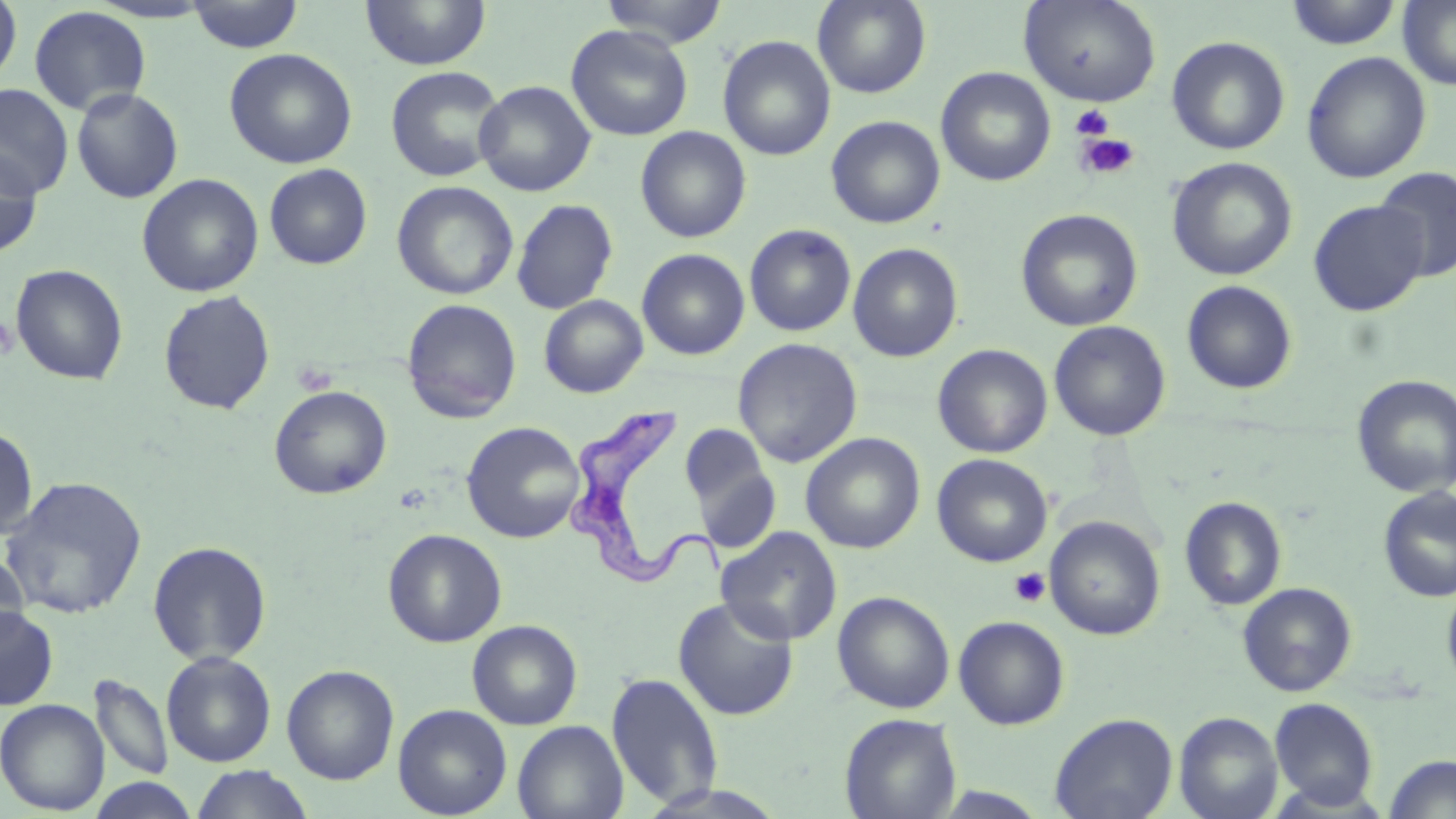
slide-level diagnosis = Trypanosoma brucei
uninfected red blood cell locations = approximate bounding boxes as [x1, y1, x2, y2] in pixels: [359, 0, 491, 71], [600, 0, 729, 48], [812, 0, 931, 98], [1284, 0, 1403, 50], [0, 1, 22, 88], [187, 1, 304, 53], [1018, 1, 1161, 107], [1398, 1, 1456, 90], [28, 5, 151, 115], [566, 24, 693, 141], [717, 35, 836, 161], [1166, 36, 1290, 155], [224, 47, 358, 169], [1301, 51, 1432, 183], [385, 65, 506, 182], [936, 66, 1056, 187], [474, 80, 596, 196], [0, 84, 74, 198], [71, 87, 184, 203], [826, 115, 945, 229], [635, 126, 751, 243], [0, 149, 42, 257], [1166, 157, 1298, 281], [263, 164, 372, 269], [1375, 166, 1456, 281], [137, 173, 264, 297], [391, 180, 519, 300], [511, 198, 618, 315], [1308, 199, 1429, 316], [1015, 208, 1144, 332], [744, 224, 856, 336], [847, 242, 963, 362], [637, 248, 750, 360], [10, 263, 128, 385], [1181, 280, 1298, 395], [158, 290, 276, 414], [539, 295, 649, 398], [401, 298, 522, 423], [1049, 320, 1171, 441], [733, 338, 862, 468], [932, 343, 1053, 458], [1352, 374, 1456, 498], [269, 385, 392, 499], [461, 421, 585, 543], [680, 422, 773, 520], [0, 425, 39, 541], [800, 432, 925, 554], [932, 453, 1052, 567], [1, 475, 147, 619], [1378, 486, 1456, 602], [1180, 496, 1287, 611], [1045, 515, 1165, 641], [716, 526, 842, 646], [382, 528, 507, 647], [147, 540, 272, 666], [0, 549, 29, 654], [1441, 579, 1456, 694], [1237, 582, 1357, 696], [832, 590, 956, 713], [673, 596, 798, 721], [0, 604, 58, 709], [953, 615, 1070, 730], [467, 620, 582, 730], [161, 651, 276, 767], [281, 664, 399, 785], [605, 671, 725, 810], [91, 674, 174, 781], [1269, 697, 1379, 810], [0, 699, 110, 815], [393, 703, 512, 818], [1174, 711, 1284, 819], [839, 712, 961, 819], [1049, 712, 1178, 819], [512, 720, 629, 819], [1383, 754, 1456, 818], [191, 765, 313, 819], [87, 778, 200, 819]
modality = light microscopy
field of view = single
preparation = thin blood smear
platelet locations = approximate bounding boxes as [x1, y1, x2, y2] in pixels: [1071, 104, 1114, 140], [1075, 132, 1140, 181], [0, 315, 18, 360], [1009, 567, 1051, 608]
Trypanosoma brucei locations = approximate bounding boxes as [x1, y1, x2, y2] in pixels: [565, 401, 720, 593]
magnification = 1000x
image size = 1456×819 pixels
stain = May-Grünwald-Giemsa